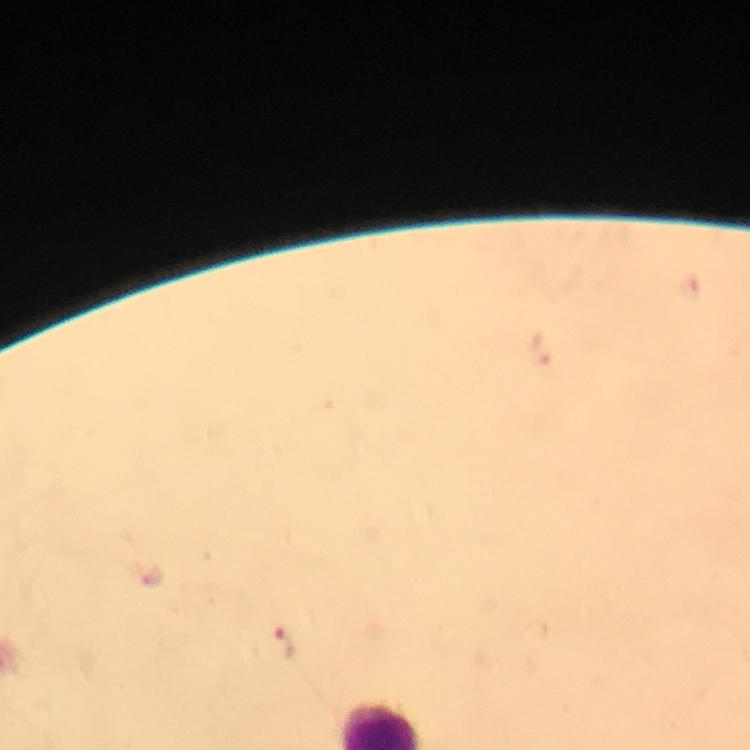
magnification: 100x
malaria_parasite_locations: 'approximate centers as (x, y) in pixels: (543, 352), (277, 644)'
immersion_oil: applied
cropped_from: one field of view
stain: Giemsa
capture: smartphone camera through the microscope
context: from a diagnostic examination for malaria
image_size: 750×750 pixels
preparation: thick blood smear